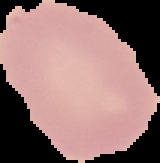

image type = segmented cell region on a black background
result = negative for malaria parasites
image size = 160×163 pixels
preparation = thin blood smear